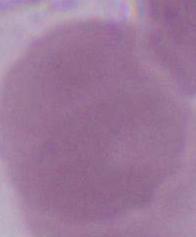

Summary:
  - Magnification: 1000x
  - Modality: photomicrograph
  - Identification: erythrocyte